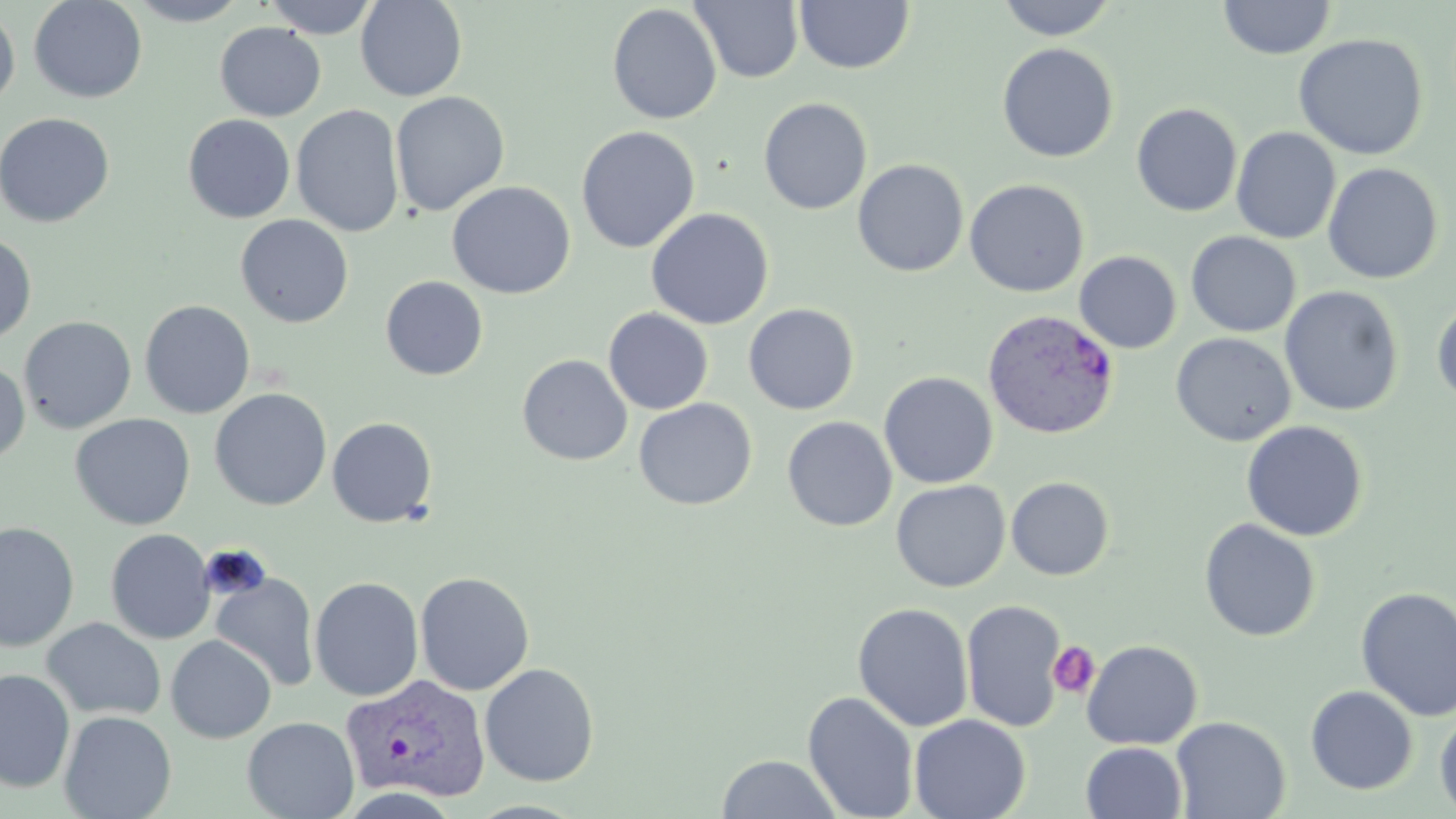

Summary:
  - Coordinate format: approximate bounding boxes as (x1,y1)-(x2,y2) corner pairs in pixels
  - Platelet locations: (1047,641)-(1101,698)
  - Plasmodium vivax-infected red blood cell locations: (982,309)-(1120,439), (340,673)-(491,804)
  - Uninfected red blood cell locations: (29,0)-(147,103), (124,0)-(251,26), (262,0)-(380,39), (355,0)-(467,102), (689,0)-(804,83), (996,0)-(1119,40), (794,1)-(915,74), (1217,1)-(1337,60), (607,4)-(722,125), (0,6)-(20,111), (215,22)-(326,121), (1293,33)-(1429,160), (997,43)-(1119,162), (390,91)-(510,216), (758,97)-(872,214), (1131,102)-(1243,217), (291,104)-(405,238), (0,112)-(115,228), (183,114)-(296,224), (576,126)-(700,254), (1231,127)-(1341,244), (852,159)-(969,277), (1322,162)-(1443,284), (964,179)-(1089,298), (446,180)-(576,299), (646,207)-(773,330), (235,214)-(354,328), (0,231)-(37,345), (1186,232)-(1302,338), (1074,251)-(1181,353), (380,276)-(488,381), (1280,286)-(1404,417), (1431,297)-(1456,405), (139,299)-(256,419), (743,304)-(859,415), (603,307)-(714,415), (19,315)-(137,434), (1171,332)-(1296,447), (517,354)-(632,466), (0,360)-(30,466), (879,371)-(998,488), (210,388)-(332,511), (634,398)-(757,510), (70,413)-(195,529), (782,416)-(897,532), (327,417)-(437,527), (1241,420)-(1369,542), (1006,476)-(1114,580), (891,479)-(1010,592), (1199,518)-(1321,642), (0,521)-(80,652), (105,528)-(216,644), (414,571)-(535,696), (211,573)-(320,691), (310,576)-(424,702), (1355,586)-(1456,722), (961,599)-(1067,732), (852,602)-(974,732), (41,617)-(167,722), (165,635)-(276,743), (1081,640)-(1203,750), (480,662)-(600,786), (1,669)-(75,793), (1305,685)-(1419,795), (802,691)-(919,819), (1435,709)-(1456,816), (58,710)-(176,819), (909,714)-(1031,819), (1171,715)-(1290,819), (242,716)-(359,819), (1081,741)-(1187,819), (716,753)-(842,818)
  - Slide-level diagnosis: Plasmodium vivax
  - Modality: optical microscopy
  - Image size: 1456×819 pixels
  - Preparation: thin blood smear
  - Stain: May-Grünwald-Giemsa
  - Field of view: single
  - Magnification: 1000x